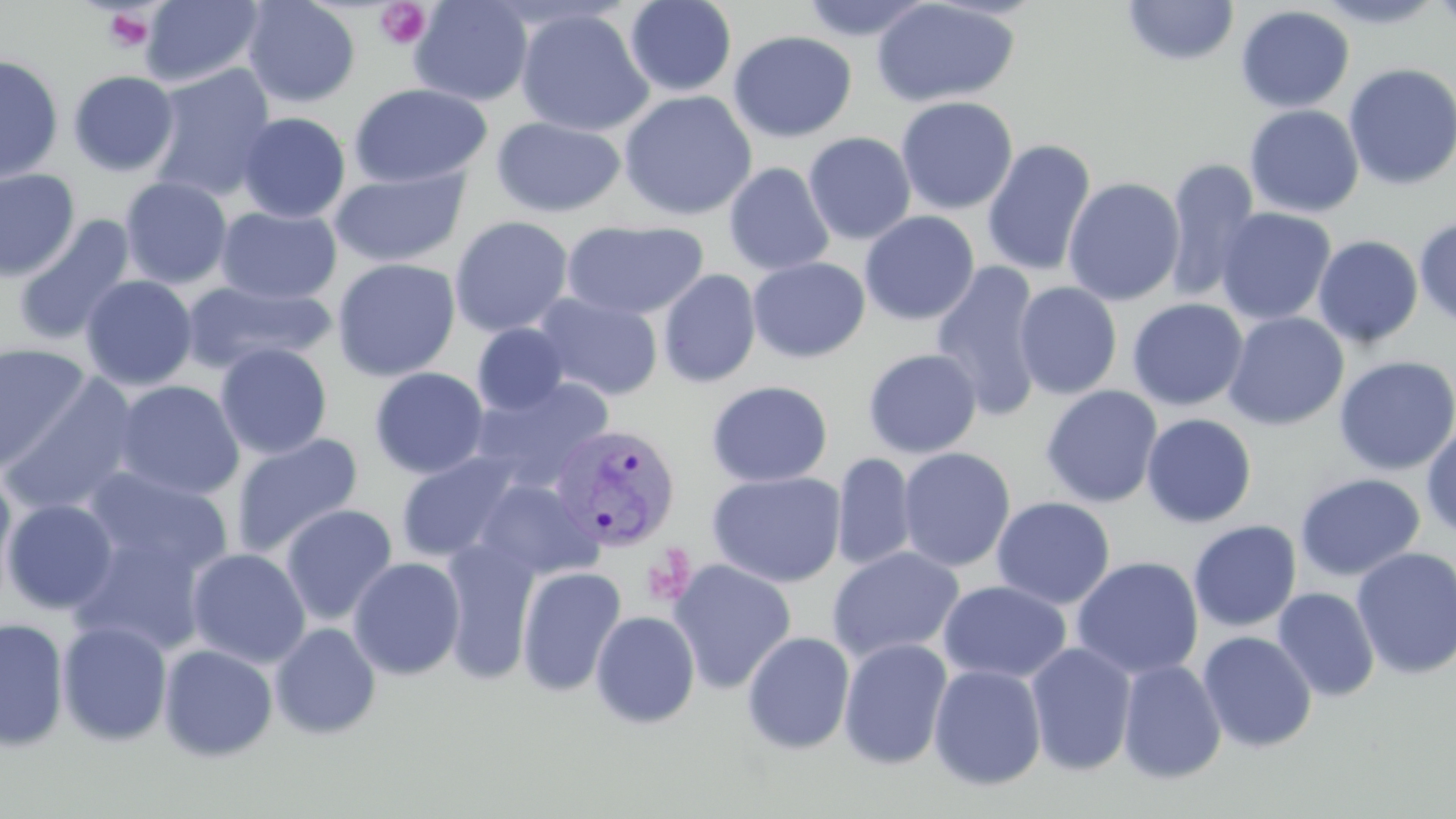 Approximate bounding boxes as (x1, y1, x2, y2) in pixels. Plasmodium vivax-infected red blood cell locations: (548, 422, 682, 554). Platelet locations: (374, 1, 431, 51), (101, 7, 155, 54), (641, 547, 696, 607). Uninfected red blood cell locations: (139, 0, 264, 88), (242, 0, 361, 108), (408, 0, 534, 107), (623, 0, 737, 98), (796, 0, 936, 43), (1122, 0, 1240, 66), (1309, 0, 1450, 29), (1429, 0, 1456, 35), (871, 1, 1021, 108), (1235, 5, 1355, 113), (515, 7, 654, 137), (728, 30, 857, 143), (0, 54, 64, 184), (1342, 62, 1456, 191), (147, 63, 277, 201), (68, 70, 180, 177), (348, 83, 492, 188), (619, 90, 757, 221), (896, 96, 1018, 215), (1244, 105, 1364, 218), (236, 112, 351, 224), (491, 115, 626, 218), (803, 132, 916, 245), (981, 138, 1097, 276), (1164, 158, 1261, 303), (723, 162, 835, 276), (330, 167, 470, 268), (0, 168, 80, 280), (1063, 176, 1185, 307), (120, 177, 232, 289), (215, 206, 342, 305), (1216, 207, 1336, 325), (859, 210, 980, 326), (449, 215, 574, 337), (1413, 215, 1456, 327), (13, 216, 136, 346), (560, 220, 709, 321), (1313, 235, 1423, 349), (746, 256, 871, 363), (331, 258, 461, 382), (931, 259, 1044, 422), (657, 269, 761, 388), (80, 275, 198, 391), (183, 280, 335, 373), (1014, 281, 1123, 400), (1014, 287, 1245, 403), (532, 292, 664, 401), (1127, 298, 1248, 411), (1223, 311, 1349, 430), (472, 323, 571, 416), (0, 341, 93, 474), (215, 343, 333, 460), (863, 349, 982, 458), (1333, 355, 1456, 475), (369, 367, 490, 479), (1, 372, 142, 517), (472, 377, 614, 490), (111, 380, 245, 501), (706, 380, 834, 488), (1040, 385, 1163, 508), (1141, 413, 1257, 528), (1421, 420, 1456, 542), (230, 433, 364, 558), (897, 447, 1016, 573), (395, 451, 525, 564), (831, 452, 918, 572), (79, 467, 233, 587), (0, 470, 19, 611), (708, 471, 847, 588), (1294, 473, 1426, 582), (472, 479, 602, 582), (992, 496, 1115, 609), (2, 498, 119, 614), (280, 503, 398, 626), (1188, 520, 1302, 632), (70, 527, 210, 657), (438, 538, 541, 684), (827, 546, 965, 663), (1351, 547, 1456, 681), (186, 548, 311, 668), (348, 556, 466, 681), (1071, 556, 1204, 680), (668, 559, 797, 693), (516, 565, 626, 696), (938, 580, 1072, 685), (1272, 587, 1380, 702), (590, 610, 700, 728), (0, 617, 69, 751), (56, 620, 173, 747), (269, 622, 382, 740), (1197, 630, 1318, 753), (741, 631, 855, 755), (838, 637, 953, 770), (1025, 641, 1137, 776), (158, 643, 278, 762), (1117, 659, 1227, 784), (928, 663, 1047, 791). Slide-level diagnosis: Plasmodium vivax. Image is 1456×819 pixels. May-Grünwald-Giemsa-stained preparation. Single field of view. Thin blood smear. 1000x magnification. Light microscopy.